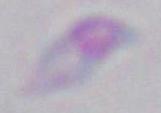
Summary:
  - Modality: micrograph
  - Identification: Toxoplasma gondii
  - Magnification: 1000x